Outline platelets.
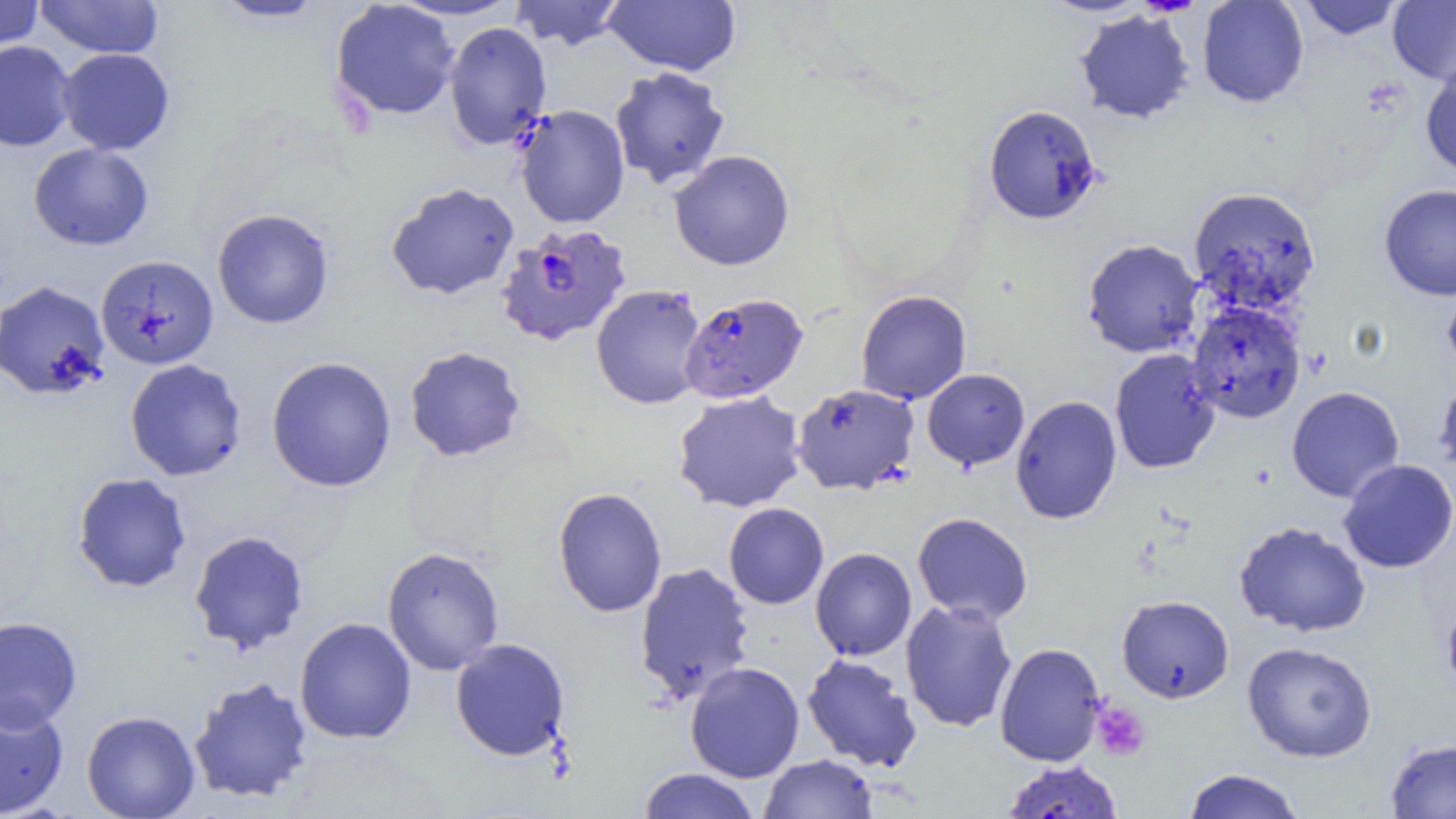
Approximate bounding boxes as (x1,y1)-(x2,y2) corner pairs in pixels.
Platelets: (1090,699)-(1151,762).

Summary:
  - Plasmodium falciparum-infected red blood cell locations: (495,223)-(632,347), (680,293)-(808,404)
  - Uninfected red blood cell locations: (0,0)-(45,53), (35,0)-(163,59), (210,0)-(330,23), (388,0)-(527,21), (509,0)-(626,51), (604,0)-(740,76), (1039,0)-(1153,16), (1197,0)-(1309,108), (1298,0)-(1404,40), (1388,1)-(1456,86), (329,2)-(461,121), (1074,9)-(1195,124), (444,21)-(552,150), (0,41)-(75,152), (57,48)-(175,155), (1420,63)-(1456,179), (609,66)-(730,190), (514,104)-(630,229), (983,104)-(1103,224), (28,142)-(153,250), (669,150)-(795,271), (386,182)-(519,300), (1379,184)-(1456,300), (1187,186)-(1321,315), (212,208)-(335,329), (1082,238)-(1204,358), (95,254)-(219,370), (1442,276)-(1456,378), (0,280)-(110,400), (590,284)-(707,410), (856,289)-(971,404), (1186,301)-(1306,424), (404,346)-(527,462), (1109,349)-(1221,474), (266,355)-(397,493), (124,359)-(247,481), (922,369)-(1030,470), (1434,374)-(1456,481), (790,383)-(920,495), (1287,386)-(1404,503), (672,390)-(807,513), (1010,395)-(1122,524), (1338,458)-(1456,573), (71,472)-(192,593), (552,487)-(667,618), (723,503)-(829,609), (913,512)-(1033,624), (1234,521)-(1371,637), (188,529)-(310,653), (381,546)-(505,675), (811,547)-(917,661), (634,562)-(756,704), (1117,594)-(1234,703), (1441,596)-(1456,699), (900,599)-(1017,732), (0,615)-(83,731), (294,617)-(417,744), (450,638)-(570,761), (994,642)-(1106,766), (1242,642)-(1377,762), (802,653)-(922,772), (685,661)-(805,782), (188,675)-(313,804), (0,698)-(69,817), (81,710)-(200,819), (1385,738)-(1456,818), (759,753)-(878,818), (1000,760)-(1125,819), (637,768)-(760,819), (1182,768)-(1305,819)
  - Slide-level diagnosis: Plasmodium falciparum
  - Image size: 1456×819 pixels
  - Preparation: thin blood smear
  - Modality: optical microscopy
  - Field of view: one of a larger specimen
  - Magnification: 1000x